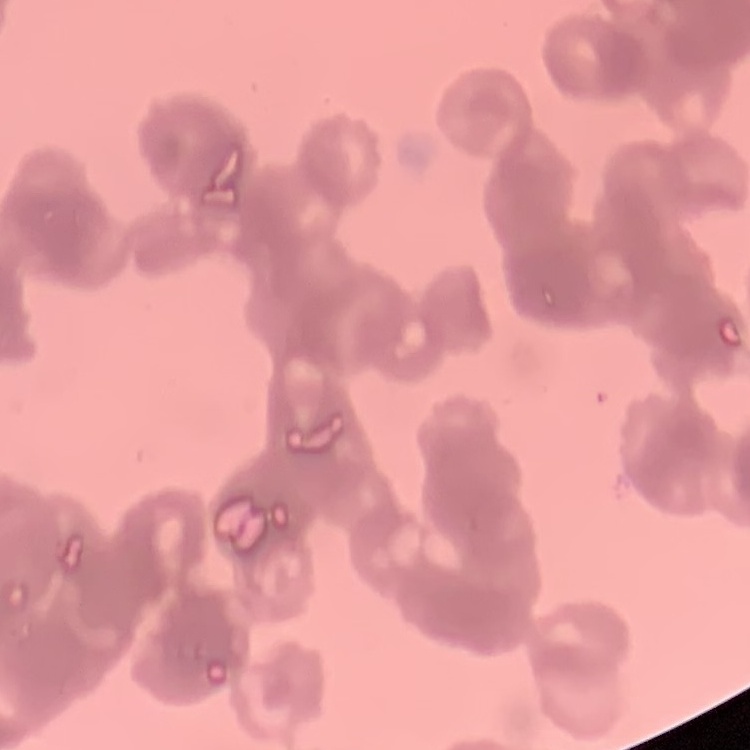

{
  "erythrocyte_morphology": "rouleaux formation",
  "image_type": "one tile cut from a larger photomicrograph",
  "stain": "Field's or Giemsa",
  "preparation": "thin blood film"
}